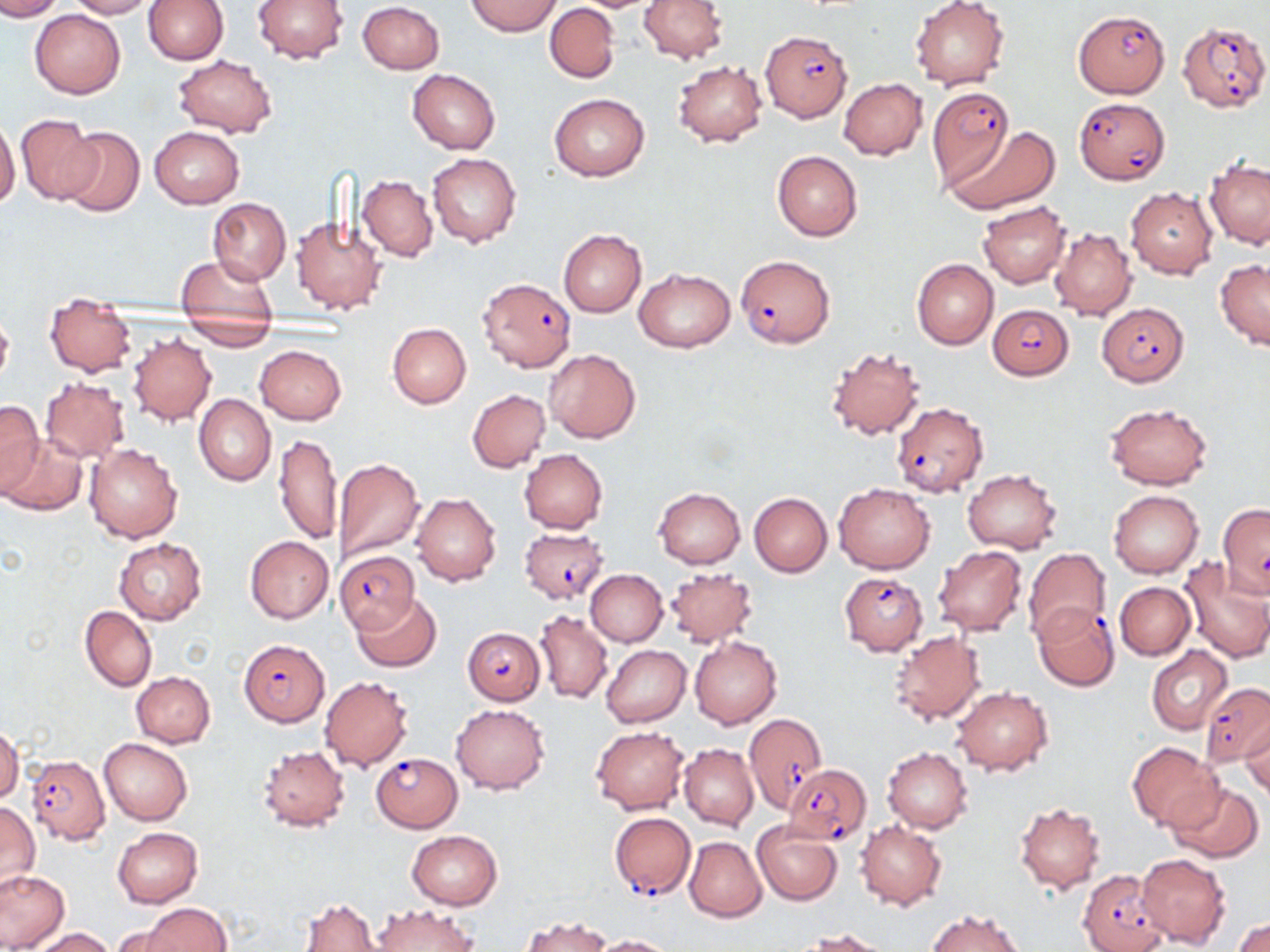
slide-level diagnosis = Plasmodium falciparum
modality = optical microscopy
image size = 1270×952 pixels
uninfected red blood cell locations = approximate bounding boxes as named x1/y1/x2/y2 corners in pixels: (x1=0, y1=0, x2=64, y2=20), (x1=66, y1=0, x2=153, y2=19), (x1=143, y1=0, x2=228, y2=64), (x1=252, y1=0, x2=350, y2=64), (x1=466, y1=0, x2=561, y2=36), (x1=639, y1=0, x2=727, y2=63), (x1=357, y1=1, x2=445, y2=73), (x1=909, y1=1, x2=1008, y2=90), (x1=545, y1=4, x2=620, y2=82), (x1=29, y1=9, x2=126, y2=98), (x1=173, y1=54, x2=277, y2=137), (x1=671, y1=60, x2=767, y2=147), (x1=407, y1=69, x2=500, y2=154), (x1=839, y1=77, x2=927, y2=160), (x1=549, y1=92, x2=650, y2=182), (x1=15, y1=115, x2=102, y2=202), (x1=0, y1=118, x2=20, y2=210), (x1=56, y1=125, x2=145, y2=218), (x1=148, y1=125, x2=245, y2=208), (x1=951, y1=126, x2=1058, y2=213), (x1=772, y1=150, x2=862, y2=240), (x1=427, y1=152, x2=521, y2=248), (x1=1205, y1=157, x2=1270, y2=248), (x1=358, y1=175, x2=438, y2=261), (x1=1125, y1=187, x2=1217, y2=278), (x1=207, y1=198, x2=290, y2=282), (x1=977, y1=200, x2=1071, y2=287), (x1=291, y1=214, x2=388, y2=314), (x1=1050, y1=227, x2=1135, y2=320), (x1=558, y1=230, x2=646, y2=317), (x1=176, y1=254, x2=277, y2=334), (x1=1215, y1=258, x2=1270, y2=351), (x1=912, y1=259, x2=998, y2=349), (x1=633, y1=268, x2=736, y2=353), (x1=45, y1=293, x2=136, y2=376), (x1=0, y1=310, x2=14, y2=390), (x1=178, y1=316, x2=280, y2=351), (x1=387, y1=322, x2=471, y2=408), (x1=128, y1=334, x2=217, y2=425), (x1=254, y1=344, x2=346, y2=424), (x1=825, y1=345, x2=927, y2=440), (x1=544, y1=349, x2=640, y2=443), (x1=40, y1=377, x2=130, y2=463), (x1=467, y1=390, x2=549, y2=472), (x1=194, y1=394, x2=275, y2=485), (x1=0, y1=400, x2=43, y2=497), (x1=1104, y1=403, x2=1212, y2=489), (x1=273, y1=433, x2=341, y2=546), (x1=3, y1=434, x2=88, y2=516), (x1=83, y1=443, x2=182, y2=542), (x1=518, y1=448, x2=607, y2=534), (x1=332, y1=457, x2=425, y2=564), (x1=962, y1=469, x2=1062, y2=553), (x1=833, y1=483, x2=936, y2=573), (x1=654, y1=488, x2=744, y2=568), (x1=1108, y1=490, x2=1204, y2=578), (x1=410, y1=493, x2=502, y2=585), (x1=748, y1=493, x2=832, y2=577), (x1=244, y1=535, x2=333, y2=624), (x1=114, y1=538, x2=206, y2=625), (x1=934, y1=545, x2=1027, y2=635), (x1=1023, y1=547, x2=1111, y2=643), (x1=1178, y1=558, x2=1270, y2=662), (x1=585, y1=569, x2=667, y2=647), (x1=664, y1=569, x2=756, y2=647), (x1=1115, y1=581, x2=1195, y2=660), (x1=352, y1=591, x2=440, y2=673), (x1=80, y1=606, x2=156, y2=692), (x1=534, y1=611, x2=612, y2=703), (x1=887, y1=629, x2=986, y2=726), (x1=689, y1=635, x2=781, y2=729), (x1=601, y1=645, x2=691, y2=727), (x1=1147, y1=645, x2=1235, y2=734), (x1=131, y1=672, x2=215, y2=747), (x1=320, y1=676, x2=414, y2=771), (x1=950, y1=685, x2=1053, y2=775), (x1=452, y1=704, x2=549, y2=794), (x1=1240, y1=717, x2=1269, y2=800), (x1=591, y1=725, x2=690, y2=814), (x1=0, y1=726, x2=22, y2=806), (x1=99, y1=738, x2=193, y2=825), (x1=1127, y1=742, x2=1225, y2=831), (x1=680, y1=744, x2=758, y2=830), (x1=256, y1=745, x2=350, y2=832), (x1=883, y1=747, x2=973, y2=833), (x1=1166, y1=780, x2=1264, y2=863), (x1=0, y1=802, x2=39, y2=893), (x1=1015, y1=802, x2=1104, y2=894), (x1=752, y1=821, x2=844, y2=905), (x1=855, y1=821, x2=946, y2=910), (x1=113, y1=828, x2=203, y2=908), (x1=406, y1=830, x2=502, y2=909), (x1=685, y1=837, x2=766, y2=922), (x1=1136, y1=852, x2=1230, y2=948), (x1=1, y1=869, x2=69, y2=950), (x1=301, y1=896, x2=380, y2=952), (x1=141, y1=902, x2=233, y2=952), (x1=371, y1=903, x2=477, y2=952), (x1=927, y1=910, x2=1027, y2=952), (x1=521, y1=916, x2=611, y2=952), (x1=1233, y1=918, x2=1270, y2=952), (x1=107, y1=924, x2=188, y2=952), (x1=29, y1=927, x2=116, y2=951), (x1=805, y1=928, x2=895, y2=952), (x1=587, y1=934, x2=675, y2=952)
preparation = thin blood film
Plasmodium falciparum-infected red blood cell locations = approximate bounding boxes as named x1/y1/x2/y2 corners in pixels: (x1=1074, y1=10, x2=1170, y2=97), (x1=1178, y1=20, x2=1269, y2=112), (x1=762, y1=30, x2=853, y2=121), (x1=927, y1=86, x2=1014, y2=186), (x1=1073, y1=97, x2=1170, y2=184), (x1=735, y1=254, x2=836, y2=348), (x1=477, y1=277, x2=576, y2=372), (x1=1096, y1=302, x2=1189, y2=386), (x1=987, y1=304, x2=1074, y2=380), (x1=891, y1=402, x2=988, y2=498), (x1=518, y1=526, x2=608, y2=604), (x1=334, y1=550, x2=425, y2=643), (x1=839, y1=572, x2=929, y2=655), (x1=1032, y1=603, x2=1121, y2=691), (x1=463, y1=626, x2=546, y2=704), (x1=239, y1=640, x2=329, y2=726), (x1=1201, y1=682, x2=1269, y2=766), (x1=742, y1=713, x2=827, y2=811), (x1=371, y1=753, x2=462, y2=832), (x1=27, y1=754, x2=109, y2=843), (x1=782, y1=763, x2=872, y2=845), (x1=610, y1=812, x2=695, y2=899), (x1=1078, y1=869, x2=1167, y2=952)
stain = May-Grünwald-Giemsa
field of view = one of a larger specimen
magnification = 1000x